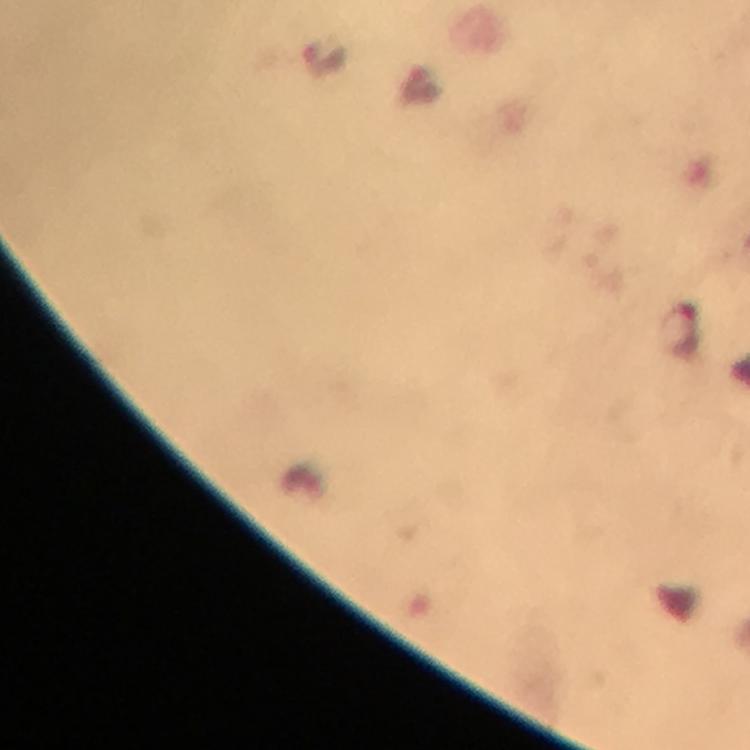

capture = smartphone mounted on the microscope
stain = Giemsa
cropped from = one field of view
context = from a diagnostic examination for malaria
image size = 750×750 pixels
malaria parasite locations = approximate centers as (x, y) in pixels: (680, 328)
magnification = 100x
immersion oil = applied
preparation = thick blood smear